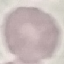

Result: no malaria parasites detected. Automatically extracted cell patch, resized to 64 × 64 pixels. Thin blood smear. Photographed with a smartphone camera at the microscope eyepiece. Giemsa-stained preparation.